Assess this cell for malaria.
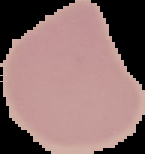
Uninfected.

From a thin blood film. Image is 145×154 pixels. Cell region segmented out of the field of view; the surrounding area is masked to black.